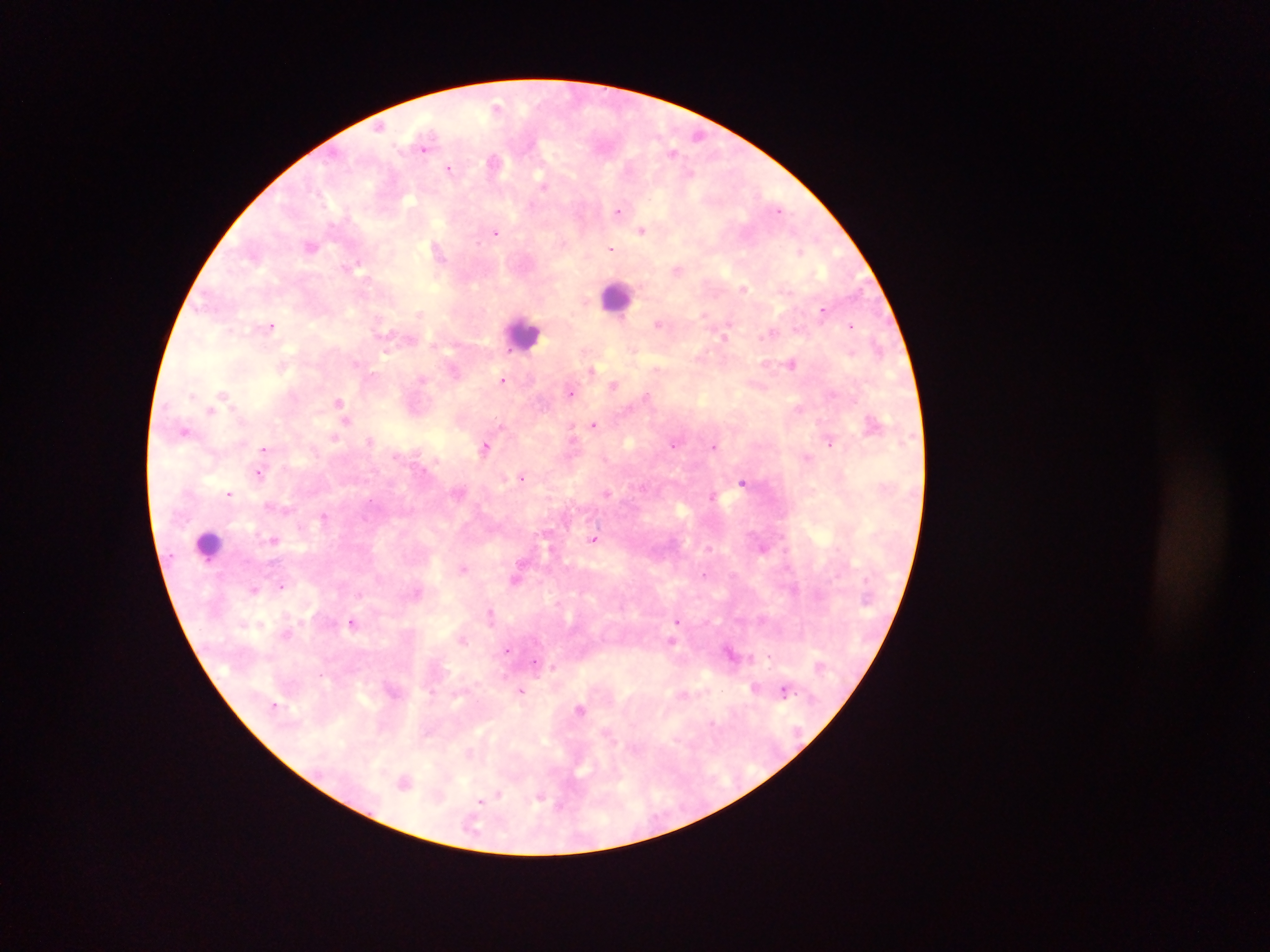

{
  "image_size": "1270×952 pixels",
  "preparation": "thick blood smear",
  "country": "Ghana",
  "malaria_parasite_locations": "approximate centers as (x, y) in pixels: (497, 105), (379, 126), (699, 135), (423, 148), (673, 151), (493, 162), (449, 168), (690, 173), (543, 185), (531, 205), (778, 209), (618, 210), (642, 230), (496, 233), (311, 245), (612, 248), (438, 251), (800, 251), (357, 265), (677, 270), (744, 288), (823, 310), (419, 313), (705, 315), (658, 324), (851, 325), (271, 326), (769, 335), (724, 336), (878, 345), (386, 352), (791, 364), (592, 370), (502, 380), (614, 385), (571, 393), (223, 394), (647, 395), (193, 396), (339, 402), (798, 409), (209, 410), (346, 421), (594, 425), (184, 431), (572, 432), (334, 438), (370, 440), (829, 441), (673, 445), (714, 446), (485, 447), (264, 449), (806, 457), (259, 474), (522, 477), (742, 481), (229, 494), (607, 494), (713, 495), (371, 500), (324, 516), (274, 540), (593, 540), (520, 562), (463, 569), (704, 574), (516, 578), (281, 585), (254, 590), (491, 614), (677, 621), (352, 622), (671, 640), (462, 641), (507, 650), (730, 653), (769, 656), (553, 667), (754, 687), (520, 690), (785, 690), (275, 705), (580, 709), (712, 723), (404, 782), (496, 796), (540, 797), (482, 802), (560, 806)",
  "field_of_view": "single",
  "capture": "mobile-phone photograph through a microscope",
  "leukocyte_locations": "approximate centers as (x, y) in pixels: (617, 297), (524, 334), (208, 545)"
}